Name the parasite shown.
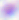
This is Toxoplasma gondii.

magnification: 400x
modality: micrograph